Classify this cell by malaria status.
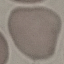

Uninfected.

Photographed with a smartphone camera at the microscope eyepiece. Thin blood smear. Giemsa-stained preparation. Automatically extracted cell patch, resized to 64 × 64 pixels.